Classify this cell by malaria status.
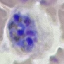
It is parasitized.

Summary:
  - Image type: cell patch, automatically extracted from a larger field of view and resized to 64 × 64 pixels
  - Capture: smartphone camera at the microscope eyepiece
  - Stain: Giemsa
  - Preparation: thin smear